Give the extent of all Plasmodium falciparum-infected red blood cells.
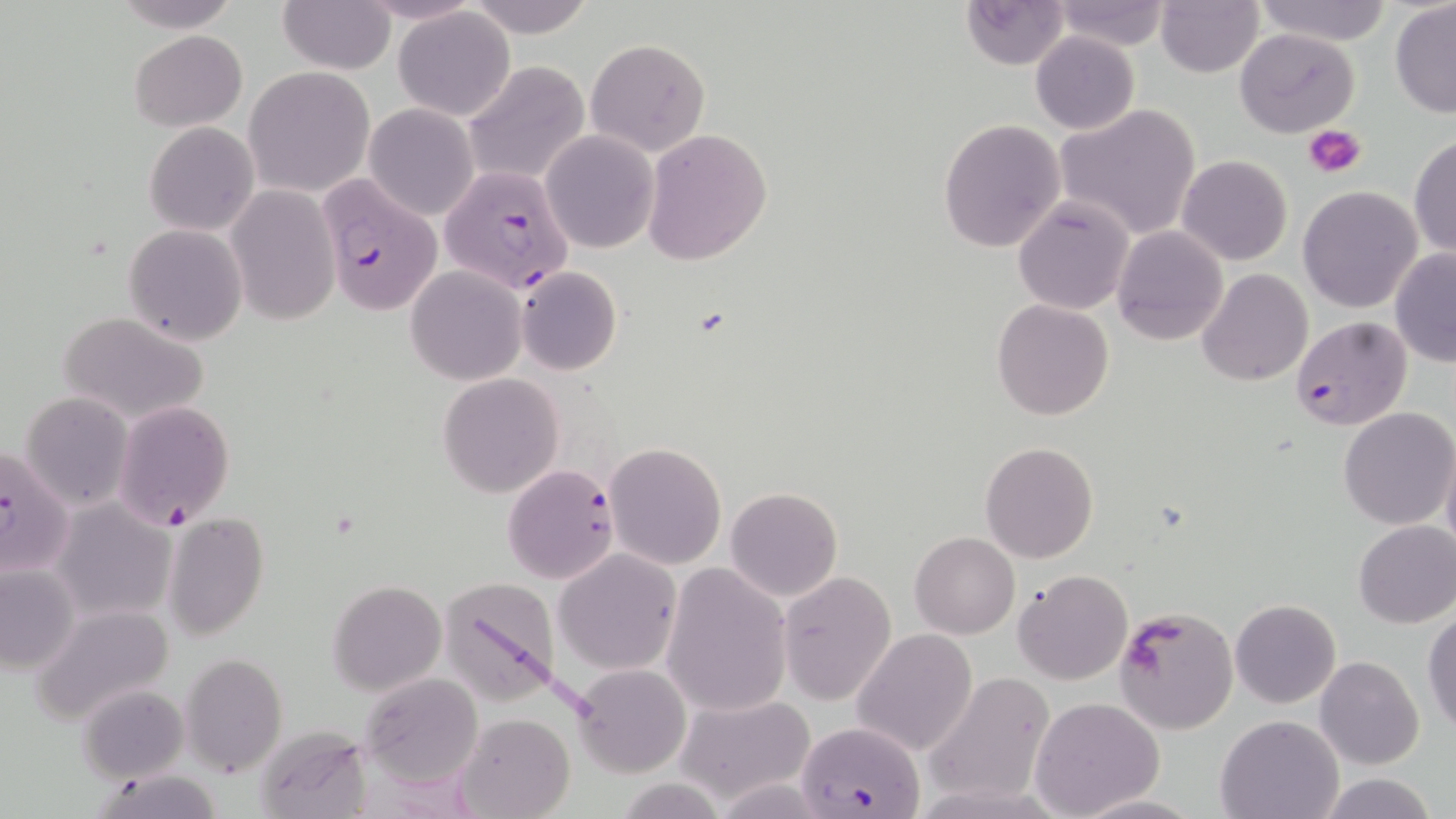
Approximate bounding boxes as (x1, y1, x2, y2) in pixels.
Plasmodium falciparum-infected red blood cells: (438, 157, 574, 292), (315, 175, 440, 316), (1290, 315, 1413, 432), (112, 400, 234, 528), (0, 441, 75, 579), (503, 465, 618, 583), (796, 721, 926, 819).

slide_level_diagnosis: Plasmodium falciparum
image_size: 1456×819 pixels
modality: optical microscopy
uninfected_red_blood_cell_locations: 'approximate bounding boxes as (x1, y1, x2, y2) in pixels: (116, 0, 238, 30), (463, 0, 598, 40), (958, 0, 1070, 70), (1048, 0, 1170, 50), (1252, 0, 1391, 46), (280, 1, 395, 74), (1157, 1, 1263, 77), (1389, 1, 1456, 118), (395, 8, 515, 121), (130, 29, 247, 130), (1234, 29, 1359, 137), (1030, 31, 1141, 135), (584, 37, 710, 156), (463, 60, 591, 189), (245, 65, 376, 196), (364, 103, 479, 220), (1053, 104, 1203, 241), (938, 117, 1066, 253), (145, 120, 259, 235), (643, 128, 771, 264), (542, 130, 658, 253), (1410, 134, 1455, 260), (1177, 155, 1292, 266), (225, 185, 340, 324), (1297, 186, 1423, 314), (1013, 196, 1135, 315), (124, 224, 248, 345), (1113, 226, 1228, 346), (1389, 248, 1456, 368), (516, 266, 621, 375), (405, 267, 526, 385), (1196, 268, 1312, 386), (991, 299, 1113, 421), (57, 311, 208, 423), (436, 373, 565, 498), (19, 391, 133, 510), (1338, 408, 1455, 529), (1441, 439, 1456, 562), (979, 441, 1100, 564), (603, 442, 727, 569), (725, 487, 844, 602), (50, 499, 177, 623), (161, 512, 270, 642), (1353, 520, 1456, 628), (909, 531, 1020, 639), (554, 549, 681, 675), (0, 563, 79, 673), (660, 564, 793, 718), (1013, 569, 1133, 685), (778, 571, 896, 706), (435, 574, 565, 709), (328, 579, 447, 697), (1231, 598, 1341, 708), (29, 602, 175, 727), (1113, 604, 1237, 735), (1423, 609, 1456, 735), (852, 628, 979, 758), (182, 653, 286, 778), (1315, 656, 1424, 769), (571, 663, 691, 778), (361, 673, 485, 789), (921, 675, 1055, 804), (79, 685, 189, 783), (675, 693, 816, 807), (1029, 697, 1164, 819), (457, 712, 576, 819), (1215, 713, 1344, 819), (250, 725, 367, 816), (93, 770, 227, 818), (1316, 773, 1440, 819), (611, 778, 732, 816), (1075, 792, 1204, 818)'
platelet_locations: 'approximate bounding boxes as (x1, y1, x2, y2) in pixels: (1306, 126, 1366, 178)'
stain: May-Grünwald-Giemsa
preparation: thin blood smear
field_of_view: one of a larger specimen
magnification: 1000x